Identify the parasite.
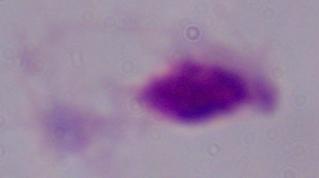
A trichomonad.

Summary:
  - Modality: photomicrograph
  - Magnification: 1000x